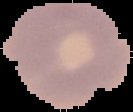
{
  "malaria_status": "parasitized",
  "image_type": "cell region segmented out of the field of view; surrounding area masked to black",
  "preparation": "thin blood film",
  "image_size": "133×112 pixels"
}